Name the cell type shown.
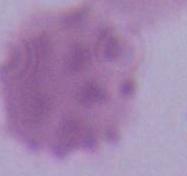
This is an erythrocyte.

Captured at 1000x magnification. Micrograph.